Report the malaria status of this cell.
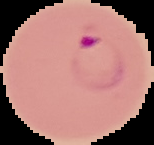
Parasitized.

From a thin blood film. Cell region segmented out of the field of view; the surrounding area is masked to black. Image is 154×145 pixels.